Describe the morphology of the red blood cells.
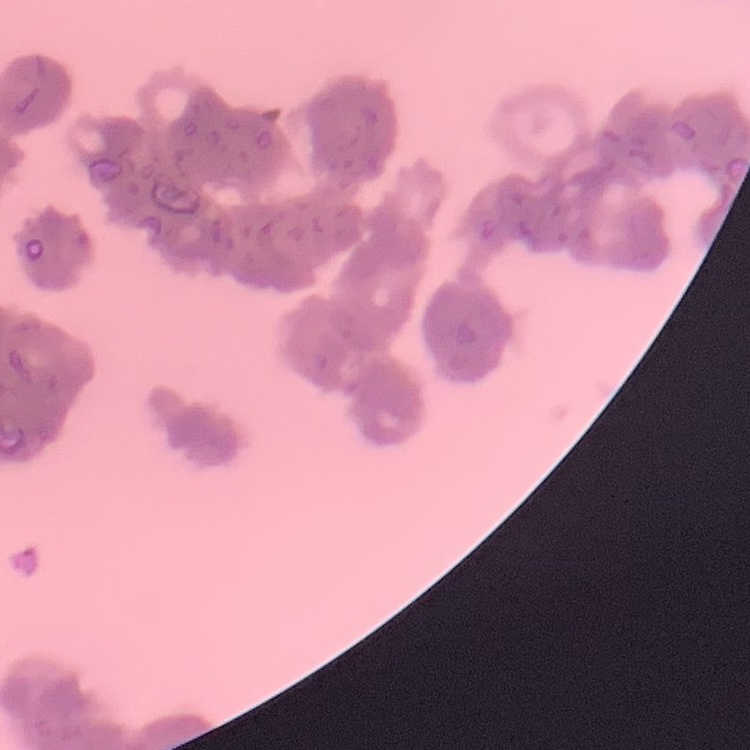

They show rouleaux formation.

stain = Field's or Giemsa
preparation = thin blood smear
image type = one tile cut from a larger photomicrograph